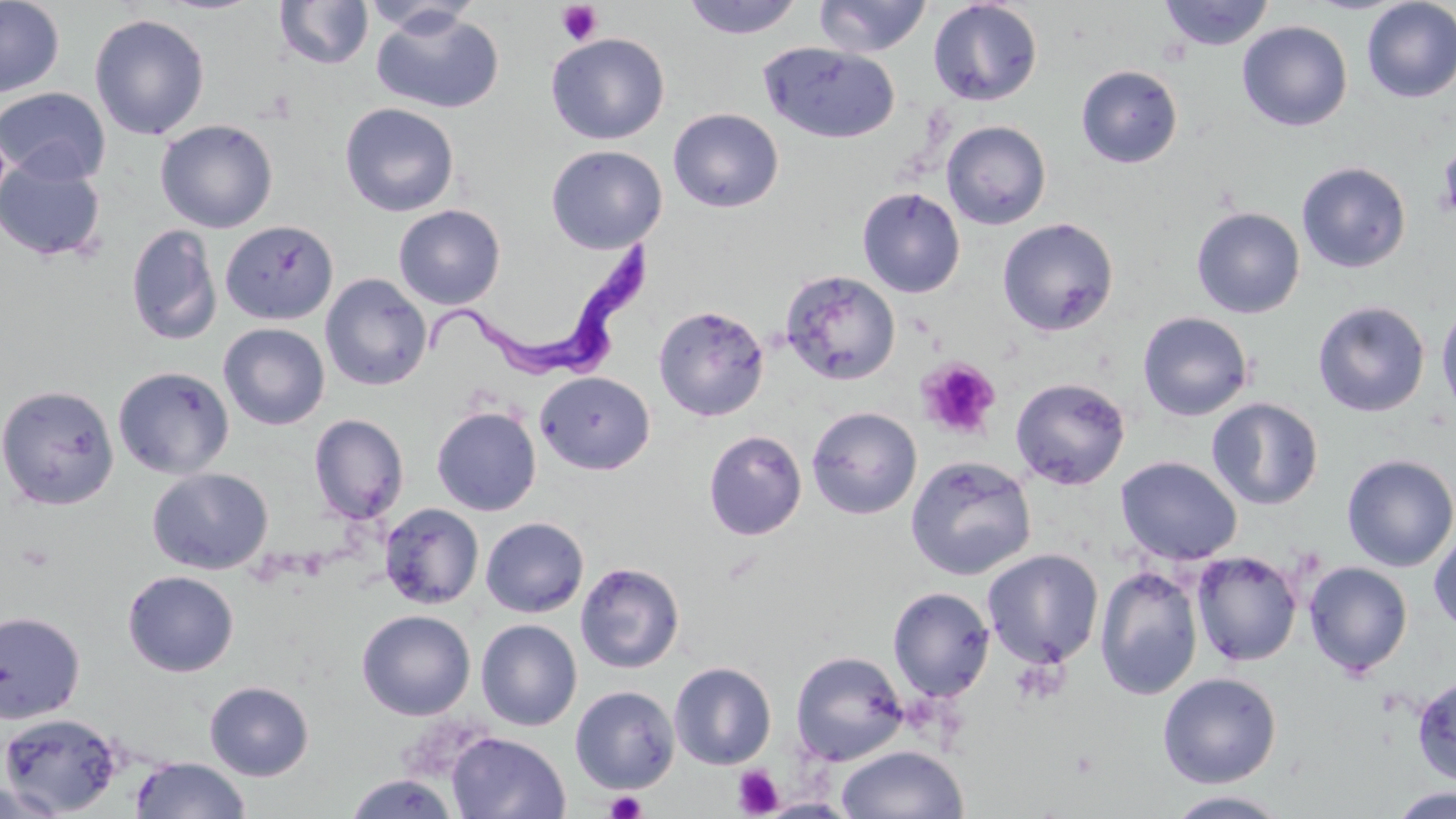

Trypanosoma brucei locations = approximate bounding boxes as named x1/y1/x2/y2 corners in pixels: (x1=408, y1=233, x2=656, y2=384)
slide-level diagnosis = Trypanosoma brucei
modality = light microscopy
image size = 1456×819 pixels
preparation = thin blood smear
stain = May-Grünwald-Giemsa
platelet locations = approximate bounding boxes as named x1/y1/x2/y2 corners in pixels: (x1=556, y1=2, x2=603, y2=47), (x1=1435, y1=141, x2=1456, y2=221), (x1=916, y1=357, x2=1000, y2=441), (x1=16, y1=540, x2=57, y2=573), (x1=733, y1=765, x2=784, y2=817), (x1=605, y1=789, x2=647, y2=819)
uninfected red blood cell locations = approximate bounding boxes as named x1/y1/x2/y2 corners in pixels: (x1=0, y1=0, x2=65, y2=98), (x1=274, y1=0, x2=373, y2=70), (x1=680, y1=0, x2=805, y2=39), (x1=814, y1=0, x2=933, y2=57), (x1=927, y1=0, x2=1043, y2=106), (x1=1157, y1=0, x2=1275, y2=51), (x1=1360, y1=0, x2=1456, y2=103), (x1=361, y1=1, x2=482, y2=37), (x1=371, y1=8, x2=504, y2=115), (x1=89, y1=13, x2=211, y2=141), (x1=1237, y1=21, x2=1352, y2=132), (x1=546, y1=33, x2=670, y2=144), (x1=759, y1=43, x2=901, y2=144), (x1=1076, y1=65, x2=1182, y2=168), (x1=0, y1=87, x2=111, y2=185), (x1=339, y1=102, x2=460, y2=217), (x1=668, y1=108, x2=784, y2=213), (x1=155, y1=119, x2=278, y2=233), (x1=941, y1=120, x2=1051, y2=230), (x1=1438, y1=139, x2=1456, y2=224), (x1=546, y1=145, x2=668, y2=253), (x1=0, y1=156, x2=107, y2=263), (x1=1297, y1=161, x2=1411, y2=273), (x1=857, y1=187, x2=965, y2=297), (x1=393, y1=204, x2=505, y2=310), (x1=1191, y1=206, x2=1305, y2=319), (x1=997, y1=217, x2=1120, y2=336), (x1=219, y1=220, x2=339, y2=325), (x1=125, y1=223, x2=222, y2=347), (x1=780, y1=270, x2=901, y2=385), (x1=320, y1=273, x2=432, y2=391), (x1=1435, y1=299, x2=1456, y2=421), (x1=1312, y1=300, x2=1430, y2=418), (x1=653, y1=304, x2=770, y2=421), (x1=1137, y1=311, x2=1254, y2=421), (x1=218, y1=323, x2=330, y2=430), (x1=112, y1=365, x2=234, y2=479), (x1=535, y1=371, x2=655, y2=475), (x1=1010, y1=376, x2=1131, y2=490), (x1=0, y1=384, x2=120, y2=510), (x1=1207, y1=397, x2=1325, y2=510), (x1=431, y1=406, x2=541, y2=516), (x1=806, y1=406, x2=922, y2=520), (x1=309, y1=414, x2=409, y2=524), (x1=703, y1=429, x2=807, y2=541), (x1=1341, y1=454, x2=1456, y2=572), (x1=906, y1=455, x2=1037, y2=580), (x1=1115, y1=455, x2=1243, y2=565), (x1=147, y1=467, x2=273, y2=574), (x1=379, y1=503, x2=484, y2=609), (x1=480, y1=517, x2=589, y2=618), (x1=1428, y1=526, x2=1456, y2=634), (x1=982, y1=549, x2=1104, y2=668), (x1=1191, y1=551, x2=1303, y2=667), (x1=575, y1=561, x2=686, y2=674), (x1=1303, y1=561, x2=1413, y2=677), (x1=1094, y1=565, x2=1204, y2=701), (x1=123, y1=571, x2=239, y2=676), (x1=887, y1=586, x2=995, y2=703), (x1=357, y1=609, x2=476, y2=720), (x1=0, y1=611, x2=86, y2=724), (x1=476, y1=619, x2=582, y2=731), (x1=790, y1=649, x2=909, y2=765), (x1=669, y1=661, x2=776, y2=769), (x1=1157, y1=672, x2=1282, y2=788), (x1=1411, y1=673, x2=1456, y2=785), (x1=204, y1=681, x2=314, y2=781), (x1=570, y1=685, x2=680, y2=794), (x1=0, y1=712, x2=124, y2=817), (x1=447, y1=731, x2=571, y2=818), (x1=836, y1=744, x2=968, y2=818), (x1=129, y1=757, x2=250, y2=819), (x1=345, y1=773, x2=457, y2=818), (x1=0, y1=779, x2=68, y2=819), (x1=1385, y1=787, x2=1455, y2=819), (x1=1163, y1=790, x2=1294, y2=818), (x1=758, y1=798, x2=859, y2=818)
magnification = 1000x
field of view = one of a larger specimen